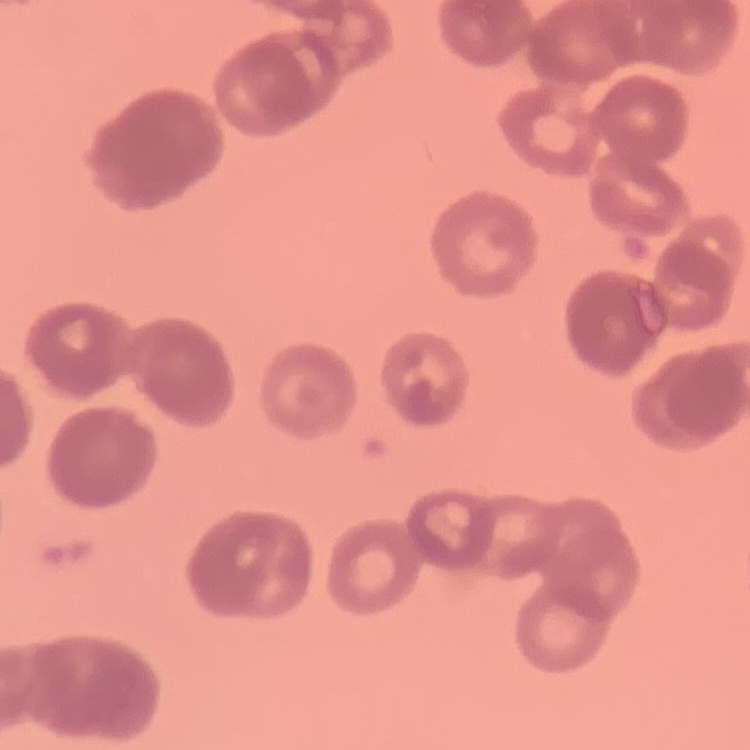

The red blood cells show rouleaux formation. Field's or Giemsa stain. Thin blood smear. Square crop of a larger photomicrograph.